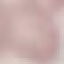
Summary:
  - Malaria status: uninfected
  - Stain: Giemsa
  - Preparation: thin blood film
  - Capture: smartphone through the microscope eyepiece
  - Image type: automatically extracted cell patch, resized to 64 × 64 pixels